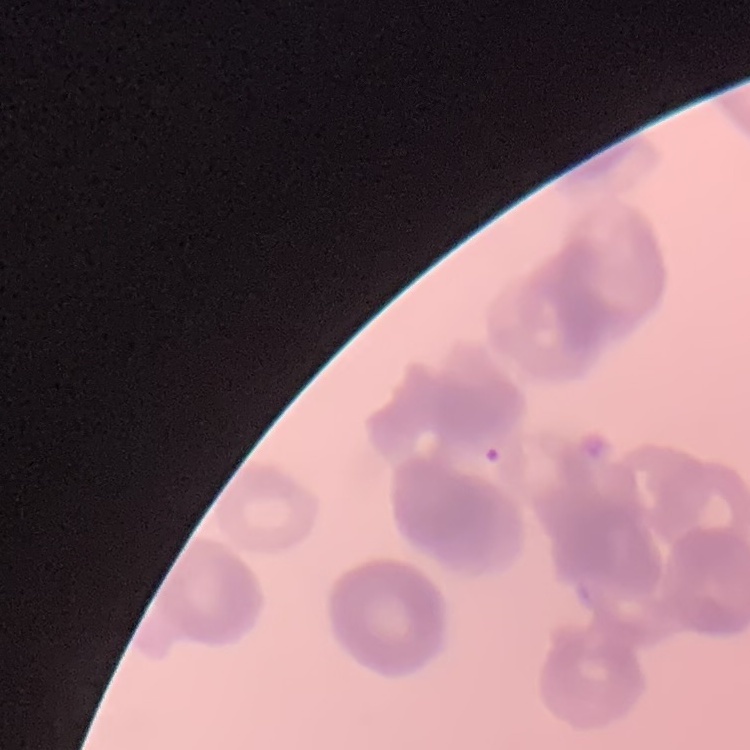

Summary:
  - Red blood cell morphology: rouleaux formation
  - Stain: Field's or Giemsa
  - Image type: one tile cut from a larger photomicrograph
  - Preparation: thin blood smear